Name the parasite shown.
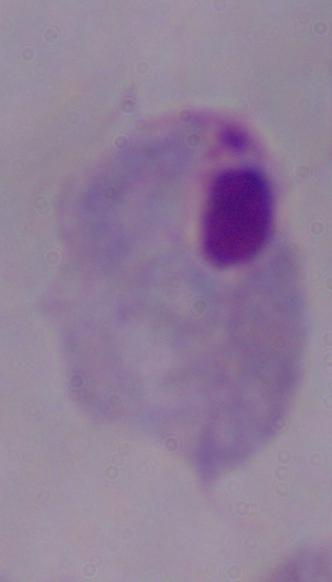
This is a trichomonad.

Summary:
  - Magnification: 1000x
  - Modality: micrograph